Identify the blood parasite species.
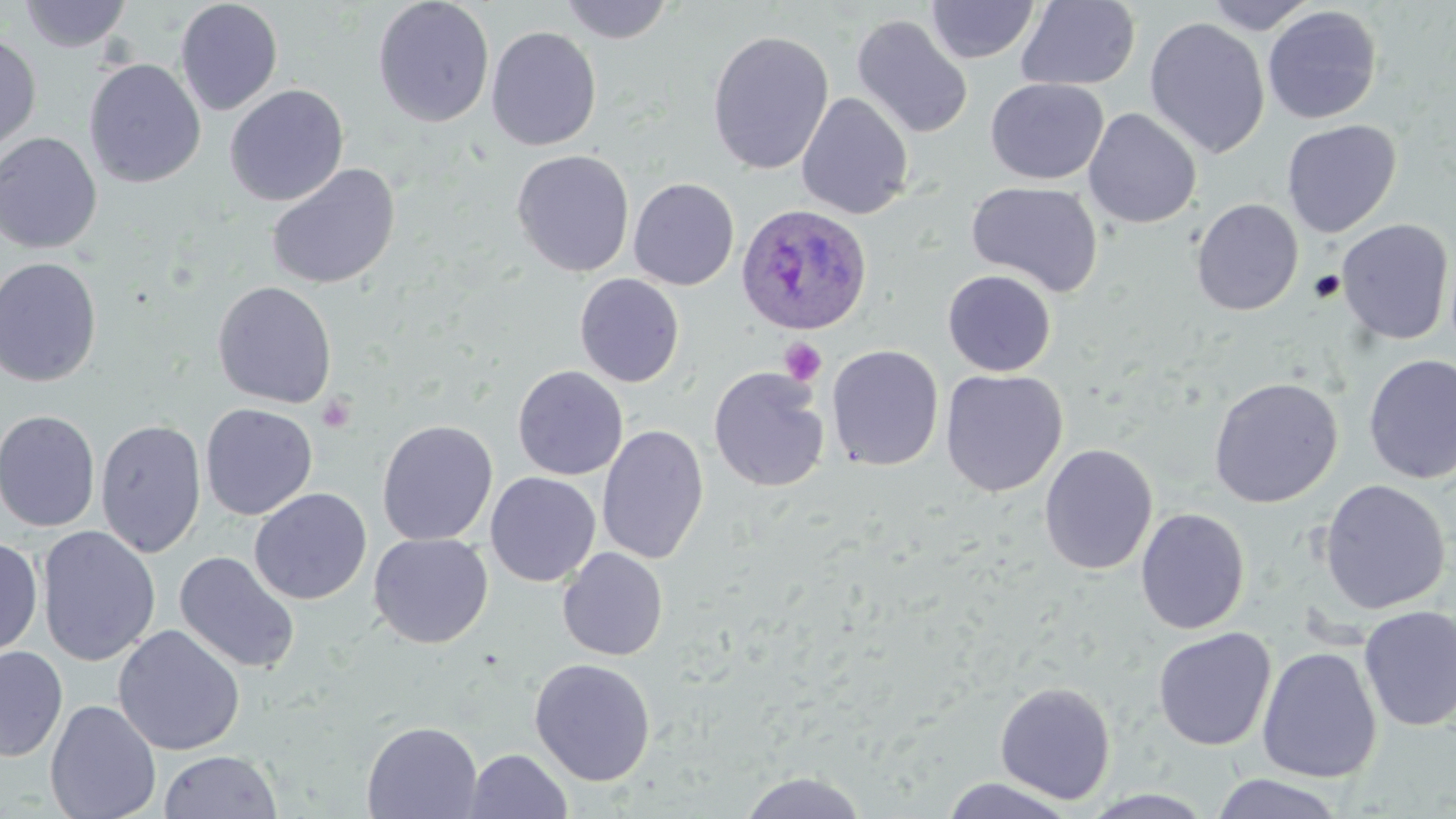

Plasmodium ovale.

Approximate bounding boxes as named x1/y1/x2/y2 corners in pixels. Uninfected red blood cell locations: (x1=18, y1=0, x2=132, y2=52), (x1=174, y1=0, x2=284, y2=116), (x1=372, y1=0, x2=494, y2=128), (x1=558, y1=0, x2=675, y2=44), (x1=925, y1=1, x2=1041, y2=64), (x1=1016, y1=1, x2=1141, y2=91), (x1=1203, y1=1, x2=1319, y2=35), (x1=1262, y1=5, x2=1383, y2=125), (x1=851, y1=14, x2=974, y2=139), (x1=1144, y1=16, x2=1270, y2=158), (x1=486, y1=25, x2=602, y2=151), (x1=706, y1=30, x2=835, y2=175), (x1=0, y1=32, x2=42, y2=156), (x1=84, y1=59, x2=206, y2=188), (x1=985, y1=78, x2=1108, y2=184), (x1=225, y1=84, x2=349, y2=207), (x1=796, y1=92, x2=914, y2=220), (x1=1083, y1=108, x2=1202, y2=228), (x1=1281, y1=119, x2=1402, y2=237), (x1=0, y1=132, x2=103, y2=254), (x1=511, y1=150, x2=634, y2=277), (x1=266, y1=164, x2=400, y2=290), (x1=628, y1=178, x2=740, y2=290), (x1=966, y1=181, x2=1103, y2=297), (x1=1191, y1=198, x2=1304, y2=316), (x1=1336, y1=219, x2=1454, y2=346), (x1=0, y1=256, x2=103, y2=387), (x1=942, y1=270, x2=1057, y2=377), (x1=574, y1=273, x2=685, y2=388), (x1=212, y1=281, x2=338, y2=409), (x1=827, y1=345, x2=944, y2=471), (x1=1363, y1=354, x2=1456, y2=485), (x1=512, y1=365, x2=628, y2=481), (x1=708, y1=367, x2=830, y2=493), (x1=940, y1=369, x2=1067, y2=497), (x1=1208, y1=376, x2=1343, y2=508), (x1=199, y1=403, x2=318, y2=520), (x1=0, y1=409, x2=101, y2=532), (x1=95, y1=419, x2=207, y2=558), (x1=377, y1=419, x2=498, y2=545), (x1=597, y1=424, x2=709, y2=565), (x1=1038, y1=444, x2=1158, y2=576), (x1=485, y1=471, x2=601, y2=587), (x1=1319, y1=479, x2=1451, y2=614), (x1=249, y1=488, x2=372, y2=605), (x1=1135, y1=508, x2=1250, y2=634), (x1=36, y1=525, x2=161, y2=667), (x1=368, y1=533, x2=494, y2=648), (x1=0, y1=535, x2=43, y2=661), (x1=557, y1=547, x2=669, y2=661), (x1=174, y1=551, x2=301, y2=674), (x1=1358, y1=605, x2=1456, y2=731), (x1=112, y1=624, x2=245, y2=756), (x1=1152, y1=627, x2=1276, y2=751), (x1=0, y1=645, x2=68, y2=762), (x1=1257, y1=646, x2=1382, y2=783), (x1=529, y1=658, x2=656, y2=786), (x1=994, y1=681, x2=1116, y2=804), (x1=45, y1=699, x2=162, y2=819), (x1=361, y1=721, x2=483, y2=818), (x1=465, y1=748, x2=573, y2=818), (x1=159, y1=750, x2=283, y2=818), (x1=738, y1=771, x2=868, y2=818), (x1=1210, y1=772, x2=1347, y2=818), (x1=941, y1=777, x2=1077, y2=818), (x1=1079, y1=789, x2=1217, y2=818). Plasmodium ovale-infected red blood cell locations: (x1=735, y1=203, x2=873, y2=336). Platelet locations: (x1=780, y1=337, x2=828, y2=386), (x1=317, y1=395, x2=356, y2=434). Light microscopy. Image is 1456×819 pixels. Thin blood film. One field of a larger specimen. 1000x magnification. May-Grünwald-Giemsa stain.